State the blood parasite species.
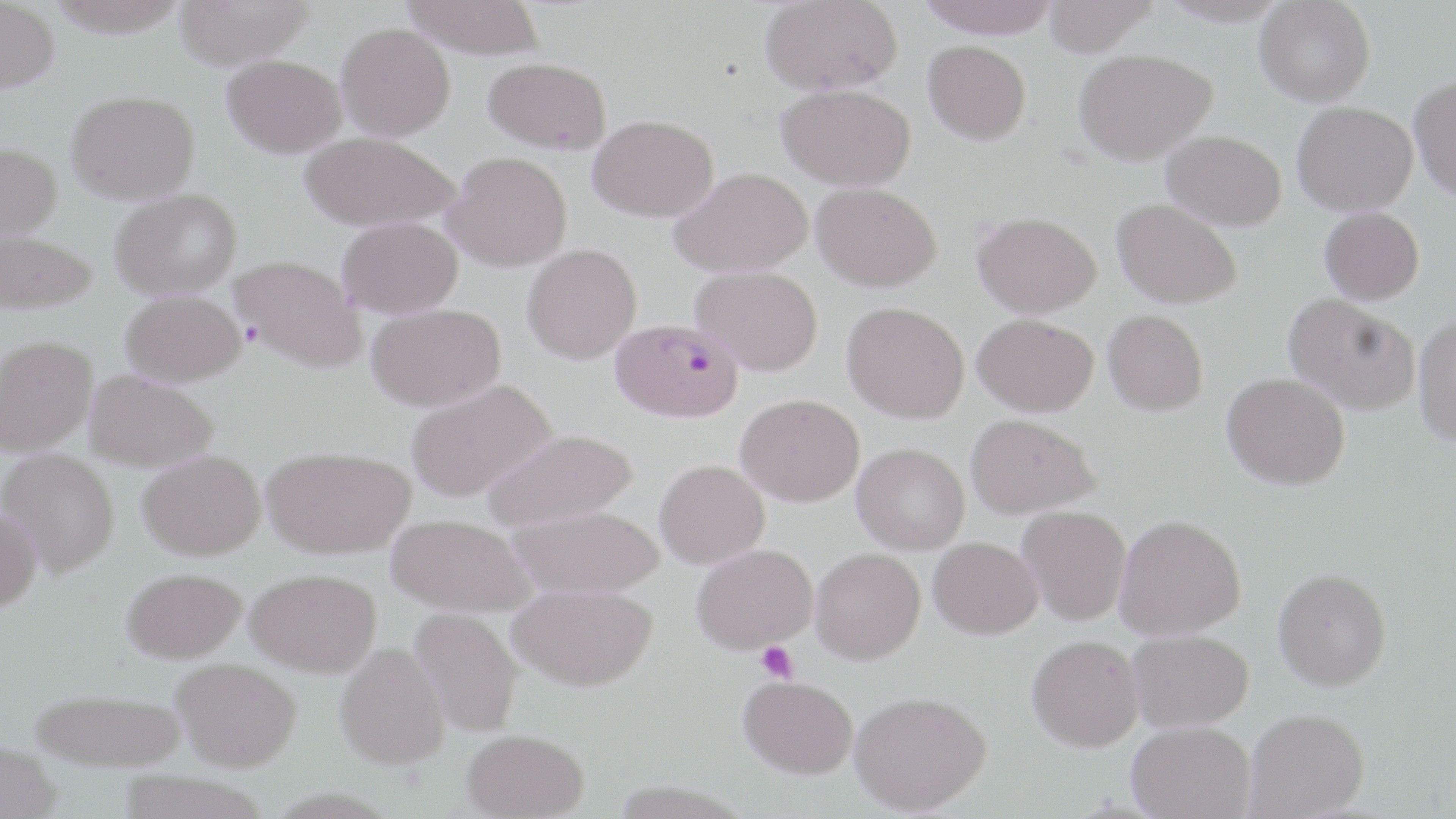
Plasmodium falciparum.

magnification = 1000x
modality = optical microscopy
stain = May-Grünwald-Giemsa
Plasmodium falciparum-infected red blood cell locations = approximate bounding boxes as (x1, y1, x2, y2) in pixels: (611, 317, 744, 422)
preparation = thin blood smear
field of view = single
uninfected red blood cell locations = approximate bounding boxes as (x1, y1, x2, y2) in pixels: (0, 0, 59, 93), (45, 0, 190, 37), (173, 0, 316, 69), (402, 0, 545, 60), (760, 0, 902, 95), (915, 0, 1061, 38), (1041, 0, 1160, 56), (1159, 0, 1292, 26), (1254, 1, 1375, 106), (335, 23, 455, 141), (922, 40, 1031, 145), (1074, 49, 1218, 165), (222, 54, 346, 158), (482, 57, 612, 153), (1409, 75, 1456, 201), (777, 83, 916, 191), (67, 90, 200, 204), (1291, 101, 1418, 216), (587, 114, 718, 222), (1162, 130, 1286, 231), (299, 132, 461, 232), (0, 142, 62, 241), (442, 151, 572, 272), (670, 168, 813, 277), (811, 181, 942, 292), (110, 188, 242, 300), (1111, 198, 1241, 308), (1319, 207, 1425, 305), (972, 211, 1101, 318), (337, 217, 462, 318), (0, 229, 98, 314), (521, 243, 642, 365), (230, 254, 366, 373), (692, 266, 824, 375), (120, 289, 245, 387), (1283, 294, 1420, 415), (841, 301, 969, 424), (366, 303, 505, 411), (1103, 309, 1208, 416), (972, 314, 1098, 417), (1413, 315, 1456, 445), (0, 334, 97, 457), (84, 369, 219, 472), (1222, 372, 1350, 490), (406, 379, 557, 502), (735, 394, 864, 506), (965, 413, 1101, 519), (482, 427, 639, 532), (851, 442, 970, 554), (262, 445, 416, 558), (1, 448, 120, 577), (137, 449, 265, 560), (654, 459, 770, 569), (507, 503, 663, 599), (1017, 505, 1131, 626), (0, 507, 41, 614), (386, 513, 537, 617), (1114, 514, 1246, 640), (928, 537, 1043, 640), (691, 544, 818, 653), (810, 548, 925, 664), (246, 567, 382, 677), (1273, 567, 1392, 691), (121, 568, 247, 663), (508, 583, 658, 691), (409, 607, 524, 736), (1127, 628, 1254, 732), (1026, 635, 1144, 752), (336, 643, 450, 770), (171, 658, 302, 771), (737, 675, 858, 779), (29, 687, 188, 771), (849, 690, 991, 814), (1244, 708, 1370, 818), (1127, 721, 1255, 818), (461, 728, 589, 819), (0, 740, 63, 819), (114, 770, 272, 819)
image size = 1456×819 pixels
platelet locations = approximate bounding boxes as (x1, y1, x2, y2) in pixels: (755, 640, 797, 683)